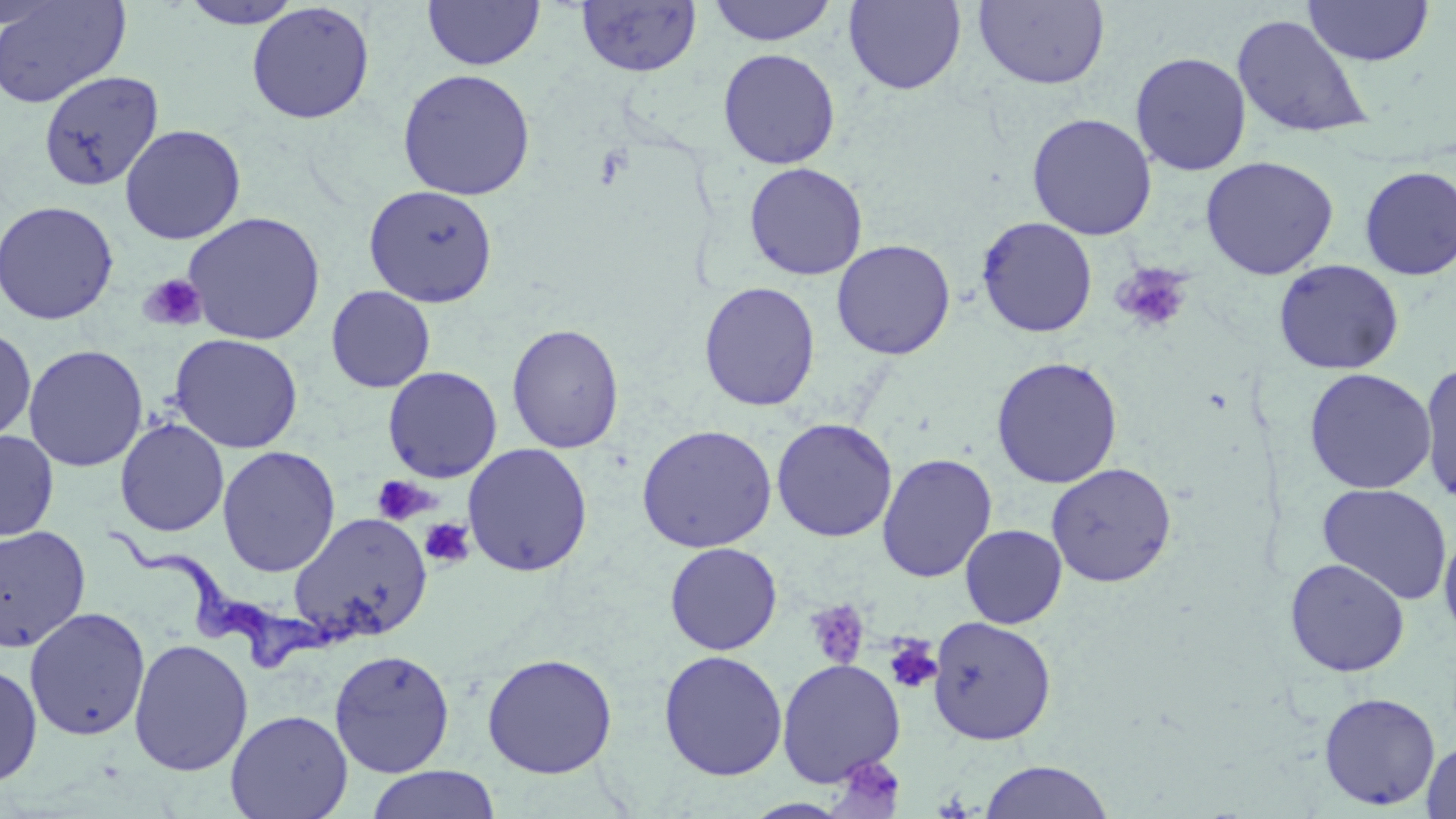
slide-level diagnosis = Trypanosoma brucei
field of view = one of a larger specimen
preparation = thin blood smear
magnification = 1000x
uninfected red blood cell locations = approximate bounding boxes as named x1/y1/x2/y2 corners in pixels: (x1=0, y1=0, x2=131, y2=109), (x1=422, y1=0, x2=545, y2=72), (x1=973, y1=0, x2=1110, y2=90), (x1=177, y1=1, x2=307, y2=29), (x1=575, y1=1, x2=701, y2=78), (x1=706, y1=1, x2=840, y2=47), (x1=843, y1=1, x2=966, y2=95), (x1=1304, y1=1, x2=1433, y2=66), (x1=245, y1=2, x2=376, y2=125), (x1=1231, y1=13, x2=1373, y2=141), (x1=717, y1=48, x2=841, y2=169), (x1=1129, y1=51, x2=1252, y2=176), (x1=397, y1=68, x2=536, y2=201), (x1=38, y1=70, x2=164, y2=191), (x1=1026, y1=113, x2=1157, y2=240), (x1=119, y1=124, x2=246, y2=245), (x1=1200, y1=156, x2=1339, y2=280), (x1=744, y1=162, x2=868, y2=280), (x1=1358, y1=166, x2=1456, y2=280), (x1=363, y1=184, x2=499, y2=307), (x1=0, y1=200, x2=119, y2=325), (x1=182, y1=211, x2=325, y2=345), (x1=977, y1=217, x2=1098, y2=338), (x1=831, y1=239, x2=956, y2=360), (x1=1273, y1=259, x2=1404, y2=375), (x1=698, y1=281, x2=820, y2=412), (x1=325, y1=286, x2=435, y2=393), (x1=506, y1=323, x2=625, y2=454), (x1=0, y1=327, x2=36, y2=443), (x1=168, y1=333, x2=304, y2=454), (x1=23, y1=344, x2=148, y2=472), (x1=991, y1=356, x2=1123, y2=489), (x1=1418, y1=362, x2=1456, y2=507), (x1=382, y1=366, x2=503, y2=483), (x1=1303, y1=368, x2=1437, y2=494), (x1=114, y1=418, x2=229, y2=537), (x1=770, y1=418, x2=897, y2=542), (x1=636, y1=423, x2=777, y2=553), (x1=0, y1=430, x2=59, y2=541), (x1=462, y1=442, x2=593, y2=577), (x1=217, y1=445, x2=340, y2=578), (x1=877, y1=453, x2=997, y2=583), (x1=1046, y1=462, x2=1177, y2=587), (x1=1316, y1=482, x2=1453, y2=605), (x1=288, y1=512, x2=432, y2=643), (x1=960, y1=524, x2=1068, y2=629), (x1=0, y1=525, x2=91, y2=652), (x1=1439, y1=528, x2=1456, y2=644), (x1=664, y1=542, x2=783, y2=655), (x1=1284, y1=558, x2=1410, y2=677), (x1=24, y1=606, x2=150, y2=742), (x1=928, y1=616, x2=1056, y2=746), (x1=128, y1=638, x2=253, y2=776), (x1=329, y1=648, x2=456, y2=777), (x1=658, y1=650, x2=787, y2=781), (x1=481, y1=652, x2=618, y2=778), (x1=776, y1=658, x2=906, y2=786), (x1=0, y1=662, x2=43, y2=787), (x1=1318, y1=692, x2=1440, y2=810), (x1=225, y1=709, x2=353, y2=819), (x1=1421, y1=738, x2=1456, y2=819), (x1=979, y1=760, x2=1113, y2=818), (x1=365, y1=766, x2=501, y2=819)
modality = light microscopy
image size = 1456×819 pixels
stain = May-Grünwald-Giemsa
Trypanosoma brucei locations = approximate bounding boxes as named x1/y1/x2/y2 corners in pixels: (x1=110, y1=530, x2=338, y2=671)
platelet locations = approximate bounding boxes as named x1/y1/x2/y2 corners in pixels: (x1=1112, y1=263, x2=1193, y2=334), (x1=139, y1=273, x2=207, y2=333), (x1=370, y1=476, x2=435, y2=526), (x1=419, y1=518, x2=476, y2=571), (x1=805, y1=599, x2=870, y2=670), (x1=884, y1=636, x2=942, y2=694), (x1=840, y1=756, x2=907, y2=800)